Identify the preparation type.
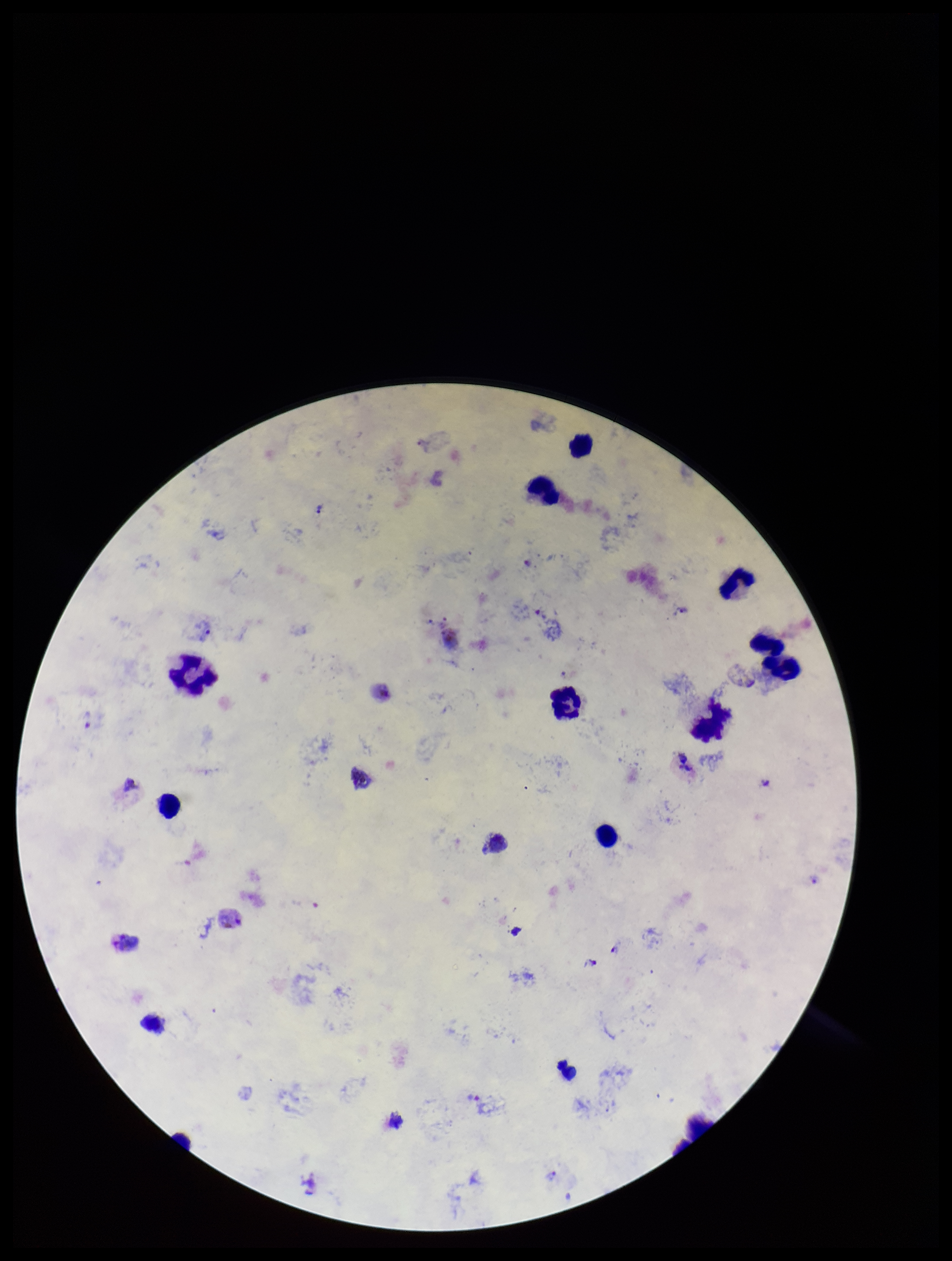

Thick.

Plasmodium parasites: seen. Leukocyte count: 12. Patient malaria status: infected. Parasite count: 5. Photographed through the microscope eyepiece with a smartphone camera. Image is 952×1261 pixels. One field from this slide. Giemsa stain. Species reported for this patient: Plasmodium vivax.